Point out malaria parasites and leukocytes.
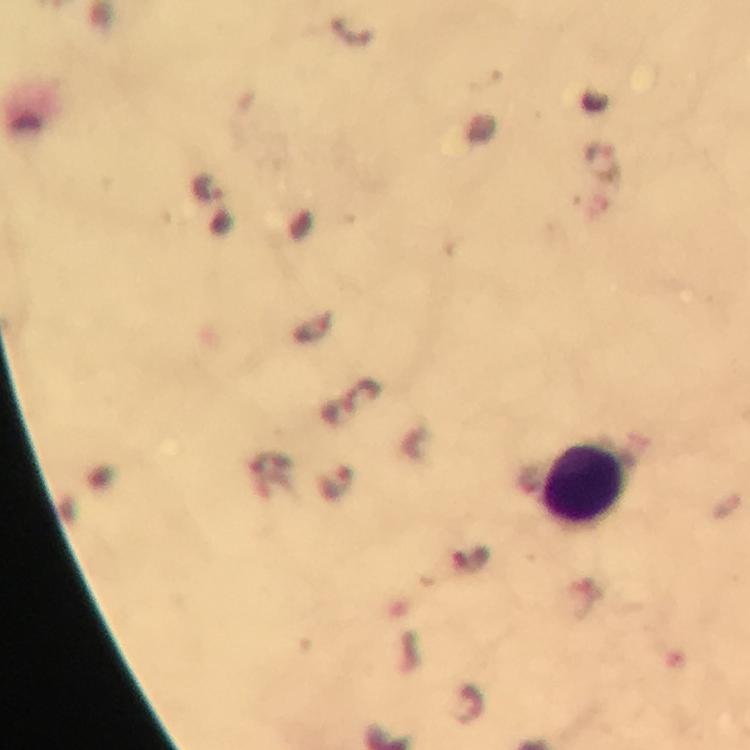

Approximate centers as {x, y} in pixels.
Malaria parasites: {604, 161}, {337, 479}.
Leukocytes: {586, 484}.

Summary:
  - Magnification: 100x
  - Cropped from: a single field of view
  - Stain: Giemsa
  - Preparation: thick smear
  - Immersion oil: used
  - Capture: smartphone camera through the microscope
  - Image size: 750×750 pixels
  - Context: from a diagnostic examination for malaria